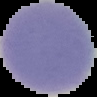
result = negative for Plasmodium parasites
image size = 97×97 pixels
image type = segmented cell region with the area outside set to black
preparation = thin blood film